Give the position of every Plasmodium parasite visible.
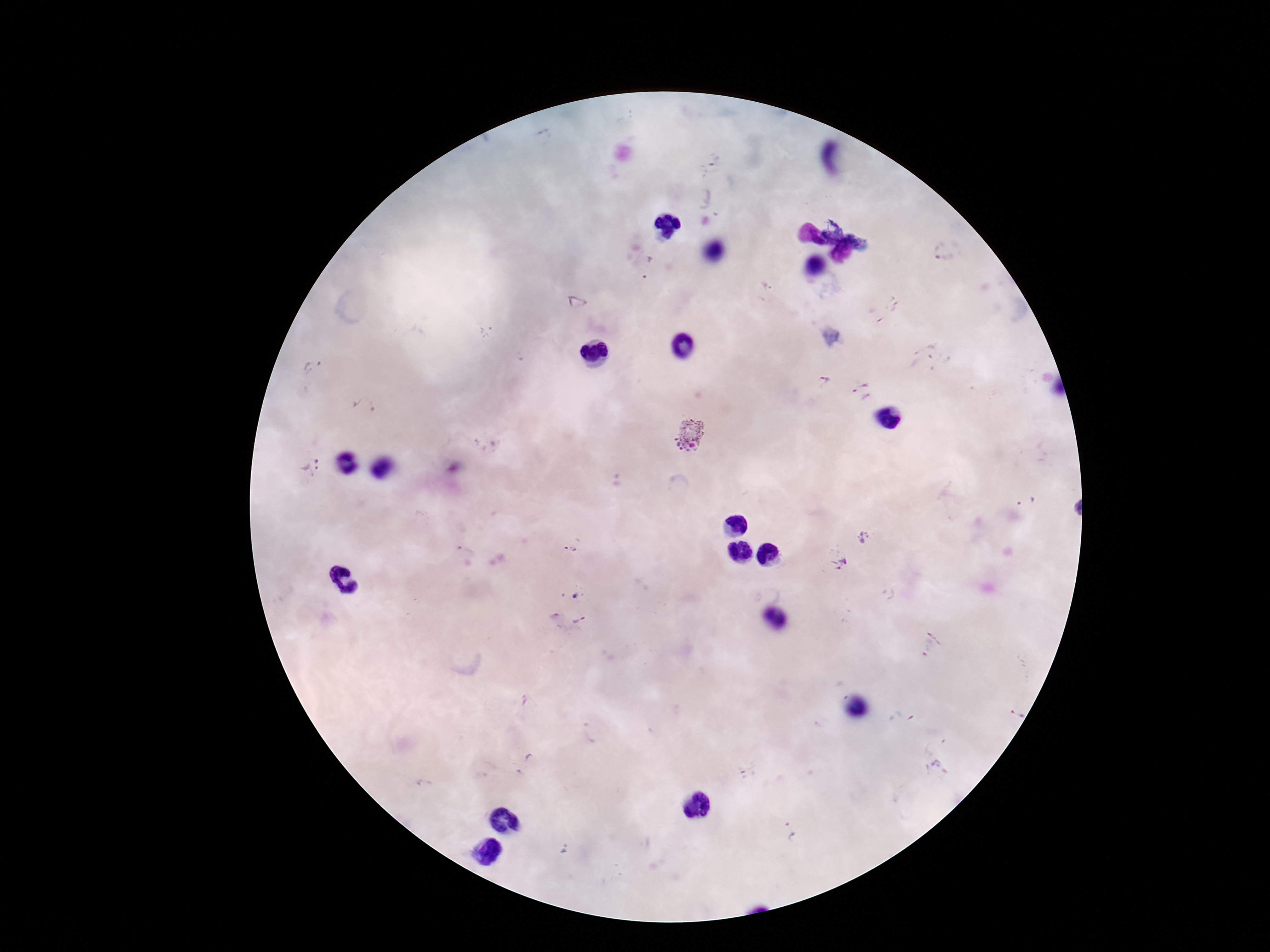

Approximate centers as {x, y} in pixels.
Plasmodium parasites: {712, 161}, {946, 251}, {650, 268}, {893, 303}, {932, 359}, {314, 367}, {824, 381}, {862, 391}, {366, 409}, {689, 434}, {309, 467}, {1026, 501}, {863, 540}, {570, 547}, {462, 551}, {839, 562}, {576, 596}, {580, 621}, {929, 643}, {524, 700}, {1016, 714}, {590, 733}, {523, 763}, {935, 769}, {791, 830}, {566, 848}.

Patient malaria status: infected. Image is 1270×952 pixels. One field from this slide. Giemsa stain. Thick blood film. Smartphone photograph taken through the microscope eyepiece. 100x magnification.